Locate every Plasmodium falciparum-infected red blood cell.
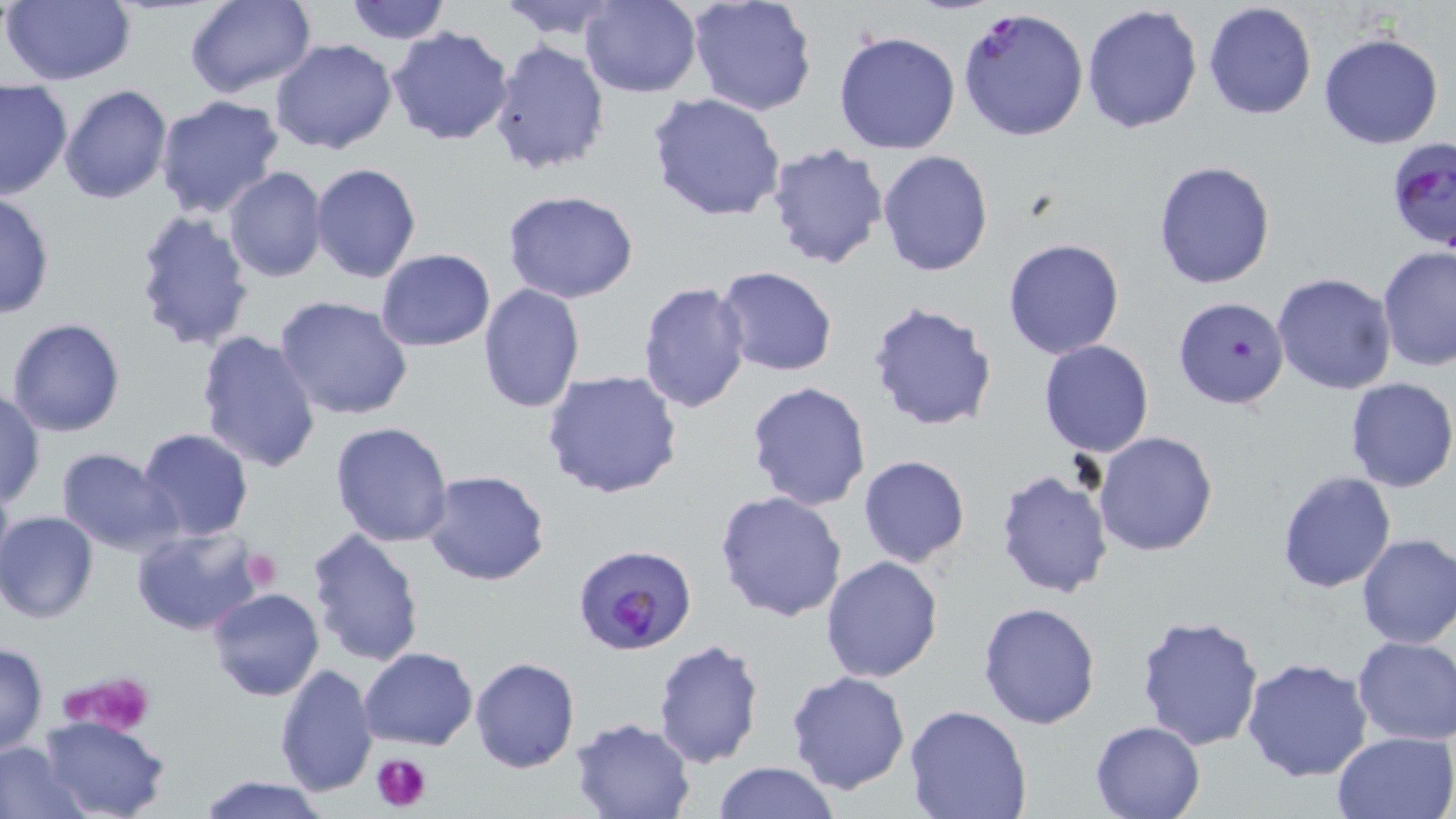

Approximate bounding boxes as [x1, y1, x2, y2] in pixels.
Plasmodium falciparum-infected red blood cells: [958, 10, 1089, 145], [1384, 135, 1456, 249], [576, 549, 699, 661].

slide-level diagnosis = Plasmodium falciparum
platelet locations = approximate bounding boxes as [x1, y1, x2, y2] in pixels: [239, 548, 283, 591], [61, 669, 158, 733], [371, 750, 432, 812]
modality = light microscopy
uninfected red blood cell locations = approximate bounding boxes as [x1, y1, x2, y2] in pixels: [3, 0, 134, 85], [183, 0, 315, 98], [344, 0, 452, 44], [496, 0, 626, 39], [579, 0, 703, 98], [688, 0, 817, 116], [1203, 2, 1317, 120], [1081, 4, 1203, 136], [386, 26, 515, 146], [833, 30, 962, 156], [1318, 33, 1445, 150], [270, 38, 399, 154], [488, 39, 611, 177], [0, 79, 72, 200], [58, 84, 174, 205], [646, 92, 788, 223], [154, 95, 286, 219], [765, 141, 888, 270], [877, 151, 995, 277], [1152, 160, 1276, 288], [311, 162, 423, 283], [223, 166, 328, 283], [502, 190, 639, 304], [0, 193, 55, 320], [131, 206, 256, 354], [1003, 237, 1126, 358], [1376, 246, 1456, 371], [374, 247, 497, 349], [715, 266, 840, 378], [1272, 273, 1397, 394], [638, 279, 752, 415], [477, 283, 587, 414], [275, 295, 414, 421], [1174, 295, 1290, 411], [867, 301, 1002, 432], [7, 318, 126, 438], [195, 329, 323, 473], [1038, 340, 1154, 456], [540, 368, 684, 500], [1344, 376, 1456, 493], [746, 380, 873, 510], [0, 388, 45, 508], [330, 421, 455, 547], [135, 428, 256, 544], [1094, 430, 1220, 558], [57, 448, 182, 556], [858, 455, 971, 569], [994, 467, 1114, 599], [0, 468, 16, 585], [421, 470, 550, 587], [1277, 471, 1396, 593], [715, 490, 848, 621], [1, 510, 99, 623], [132, 525, 265, 637], [306, 527, 426, 668], [1354, 533, 1456, 649], [820, 555, 943, 683], [206, 586, 324, 701], [977, 601, 1102, 730], [1134, 613, 1265, 752], [1350, 636, 1455, 746], [653, 638, 765, 768], [0, 641, 49, 757], [359, 647, 478, 750], [469, 656, 580, 773], [1240, 656, 1373, 782], [273, 661, 379, 798], [785, 670, 911, 793], [904, 706, 1033, 819], [38, 715, 170, 819], [569, 717, 694, 819], [1089, 719, 1208, 818], [1332, 730, 1456, 819], [0, 742, 85, 817], [713, 760, 838, 819], [197, 776, 332, 819]
magnification = 1000x
stain = May-Grünwald-Giemsa
image size = 1456×819 pixels
preparation = thin blood film
field of view = single